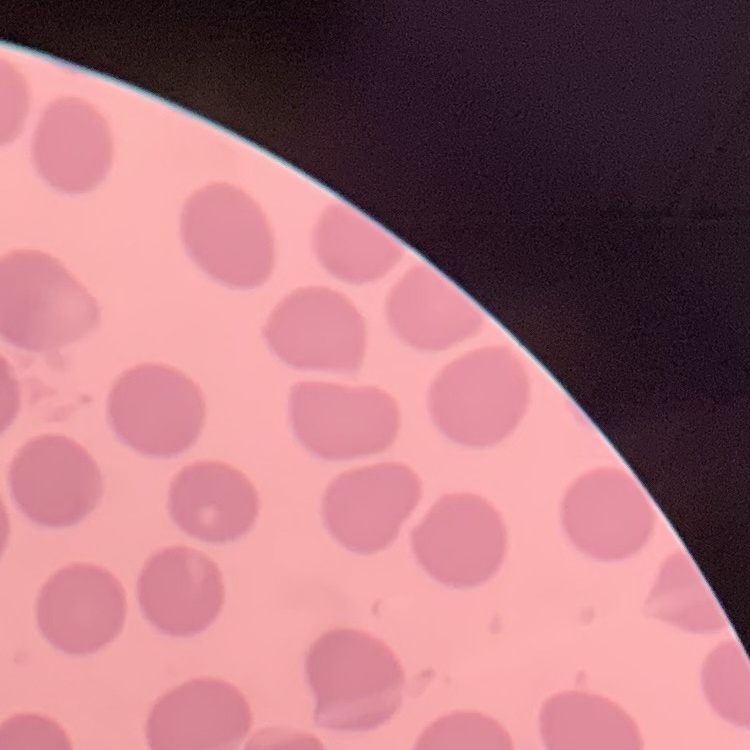 The red blood cells exhibit no rouleaux formation. One tile cut from a larger photomicrograph. Thin blood film. Stained with either Field's or Giemsa.